Assess the morphology of the erythrocytes.
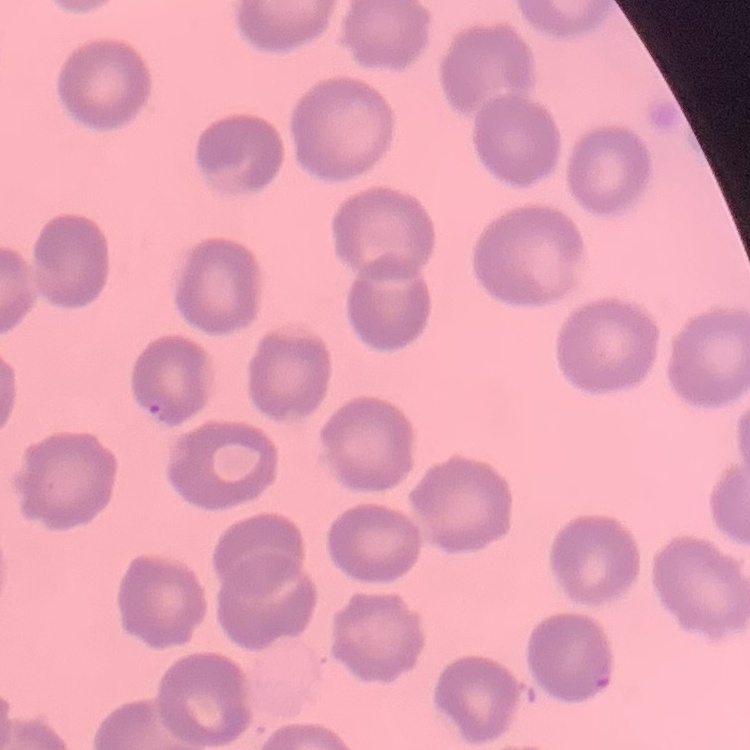

No rouleaux formation.

Square crop of a larger photomicrograph. Thin blood film. Field's or Giemsa stain.